State which parasite is depicted.
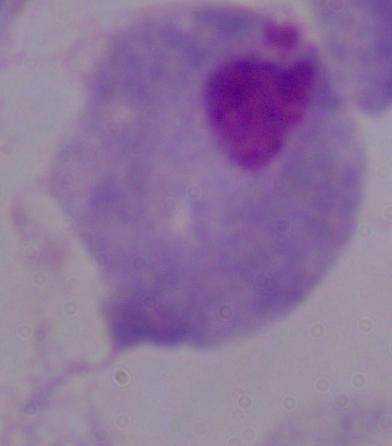
This is a trichomonad.

Micrograph. Captured at 1000x magnification.